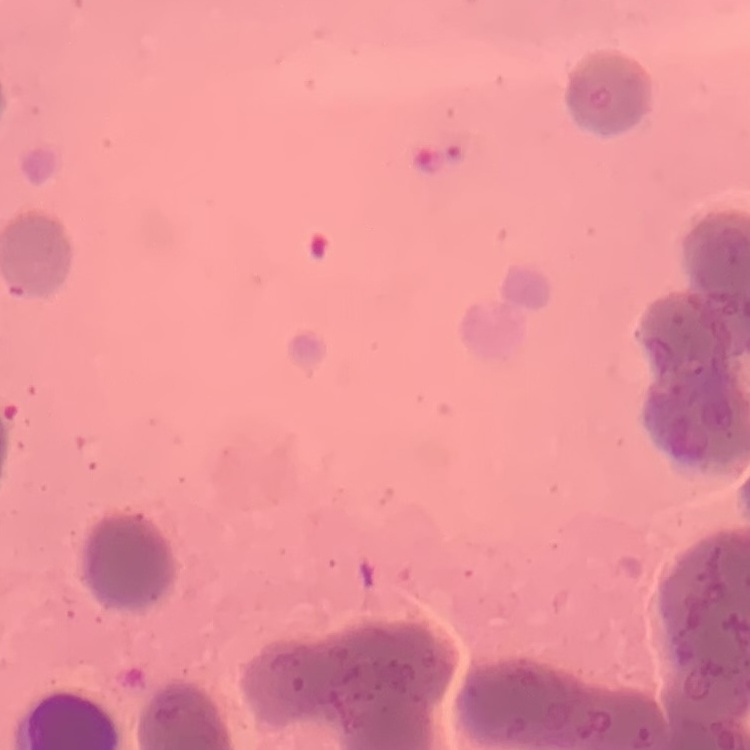

erythrocyte morphology = rouleaux formation
preparation = thin blood smear
stain = Field's or Giemsa
image type = square crop of a larger photomicrograph